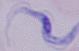

Summary:
  - Identification: trypanosome
  - Magnification: 1000x
  - Modality: micrograph